Locate every Plasmodium falciparum-infected red blood cell.
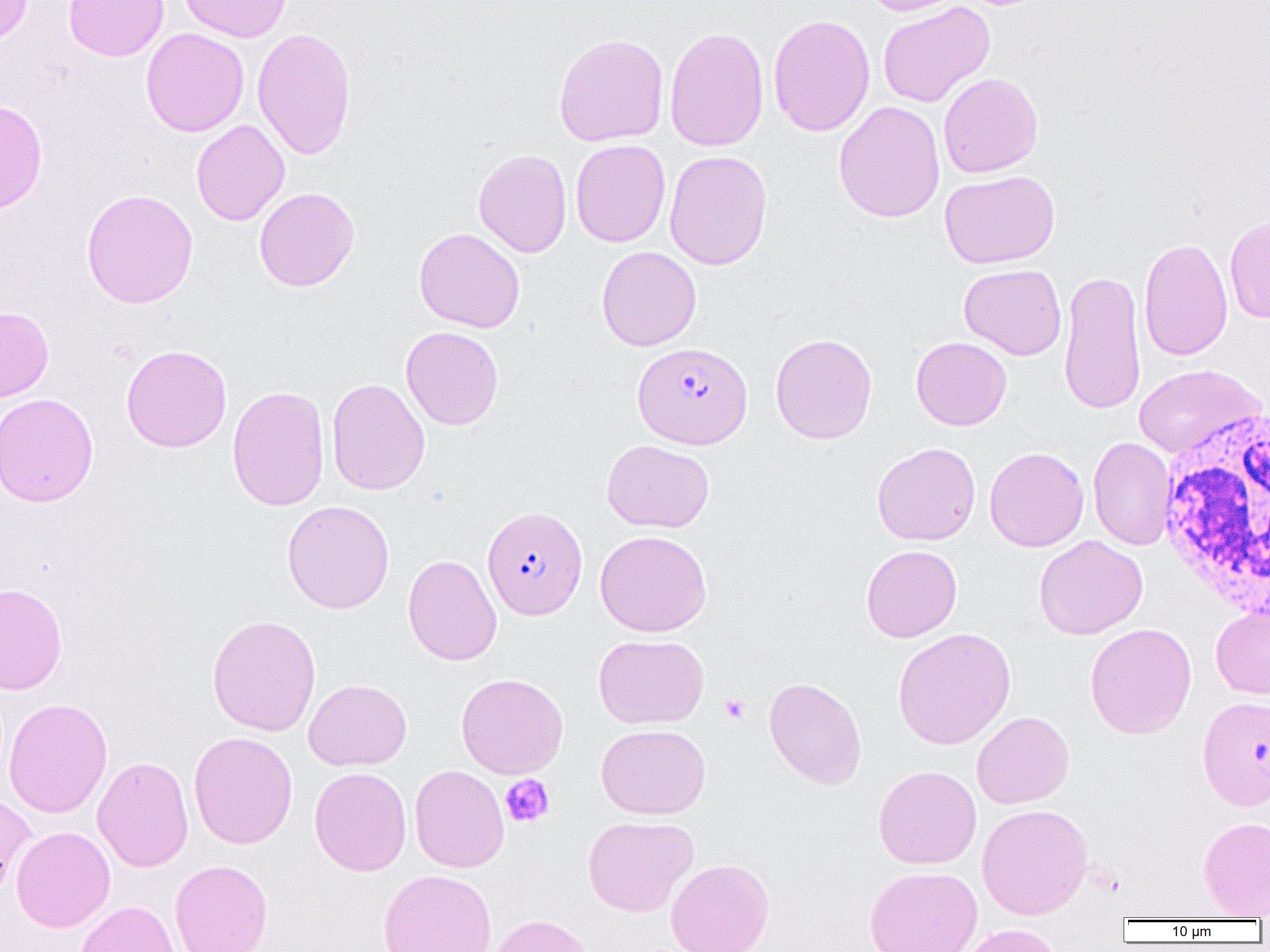
Approximate bounding boxes as (x1,y1)-(x2,y2) corner pairs in pixels.
Plasmodium falciparum-infected red blood cells: (632,342)-(753,449), (482,506)-(588,620).

Summary:
  - Uninfected red blood cell locations: (0,0)-(33,47), (63,0)-(169,61), (178,0)-(292,42), (862,0)-(965,16), (877,2)-(995,108), (768,14)-(875,137), (664,26)-(769,153), (252,27)-(357,160), (140,28)-(249,137), (553,32)-(669,147), (938,73)-(1043,178), (0,99)-(48,215), (833,101)-(945,222), (191,120)-(289,226), (570,139)-(671,247), (473,149)-(572,258), (664,149)-(773,270), (939,170)-(1060,269), (254,187)-(359,292), (81,188)-(199,309), (1224,215)-(1270,323), (414,227)-(525,333), (1138,236)-(1233,362), (596,246)-(701,351), (959,264)-(1066,360), (1058,268)-(1146,417), (0,306)-(53,403), (401,326)-(503,430), (770,333)-(877,444), (911,336)-(1011,430), (121,344)-(232,452), (1133,364)-(1267,458), (326,378)-(429,495), (227,385)-(330,511), (0,393)-(98,507), (1088,436)-(1177,551), (601,439)-(714,533), (872,442)-(981,545), (985,446)-(1089,552), (282,500)-(395,614), (595,530)-(712,637), (1034,535)-(1147,639), (861,545)-(962,642), (403,554)-(502,666), (0,582)-(68,695), (1210,605)-(1270,699), (207,614)-(321,736), (1085,623)-(1197,739), (893,627)-(1016,750), (593,634)-(709,728), (456,673)-(568,779), (764,676)-(867,789), (304,679)-(411,770), (1197,695)-(1270,810), (3,698)-(113,818), (972,711)-(1074,809), (597,723)-(710,819), (188,731)-(298,849), (92,756)-(194,872), (409,765)-(509,873), (874,765)-(982,869), (310,767)-(412,876), (0,790)-(36,896), (976,803)-(1093,919), (582,815)-(698,917), (1197,817)-(1270,918), (11,826)-(115,933), (666,858)-(774,952), (170,859)-(272,952), (864,865)-(983,952), (378,869)-(497,952), (75,900)-(180,952), (487,913)-(597,952), (959,924)-(1065,952)
  - White blood cell locations: (1157,408)-(1270,623)
  - Platelet locations: (720,695)-(749,722), (500,774)-(554,827)
  - Slide-level diagnosis: Plasmodium falciparum
  - Field of view: single
  - Modality: light microscopy
  - Preparation: thin blood smear
  - Image size: 1270×952 pixels
  - Magnification: 1000x